Report the malaria status of this cell.
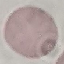
Uninfected.

Photographed with a smartphone camera at the microscope eyepiece. Thin smear of blood. Giemsa stain. Cell patch, automatically extracted from a larger field of view and resized to 64 × 64 pixels.